Locate every uninfected red blood cell.
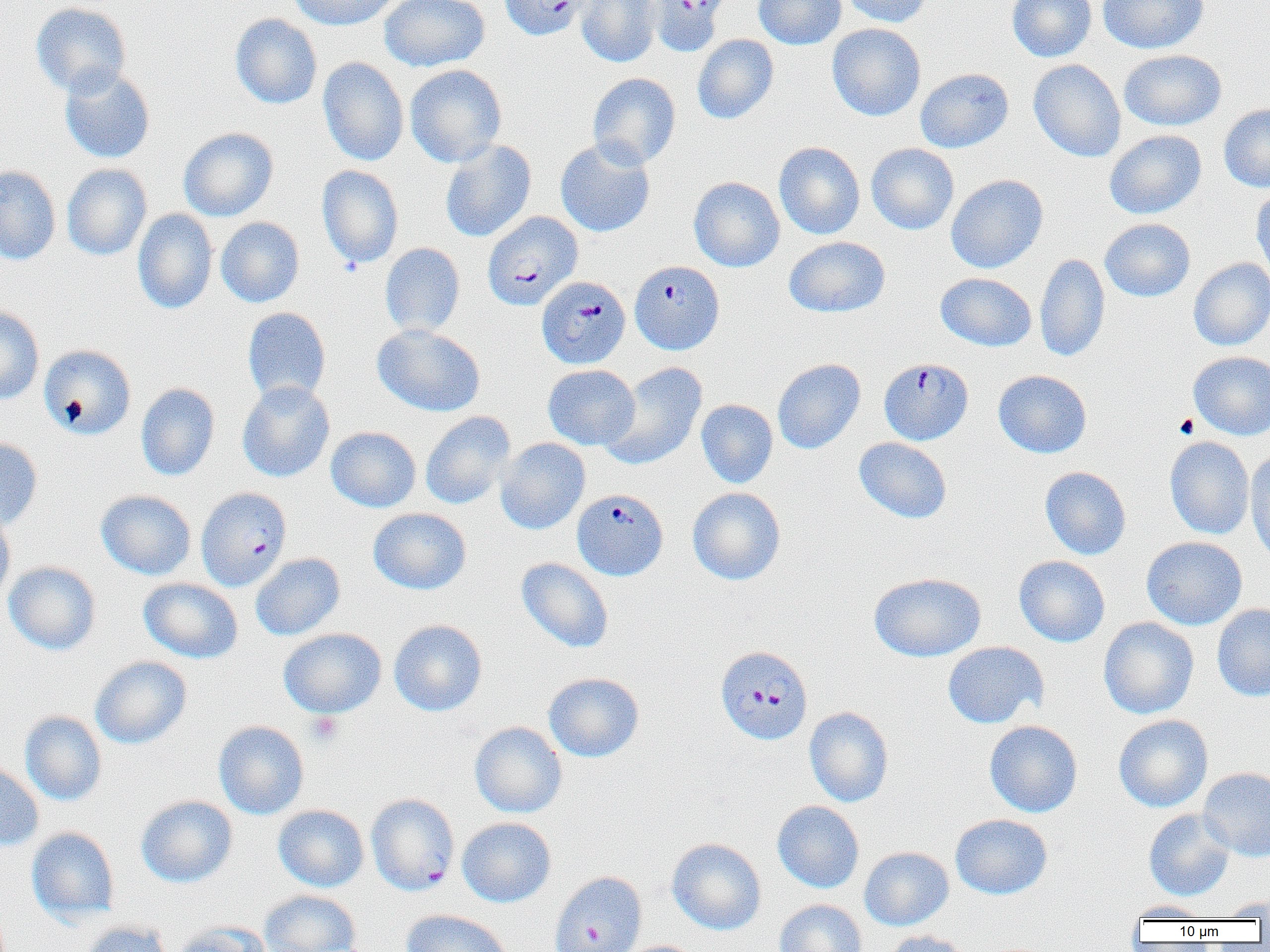
Approximate bounding boxes as (x1,y1)-(x2,y2) corner pairs in pixels.
Uninfected red blood cells: (288,0)-(402,30), (379,0)-(490,72), (577,0)-(661,68), (753,0)-(846,49), (840,0)-(931,27), (1007,0)-(1097,62), (1098,0)-(1209,54), (30,2)-(131,97), (230,14)-(322,109), (827,23)-(926,121), (692,34)-(779,124), (1119,49)-(1226,131), (318,57)-(409,167), (1028,59)-(1126,162), (405,64)-(507,167), (59,66)-(156,163), (915,68)-(1014,153), (587,73)-(681,169), (1218,104)-(1270,192), (179,127)-(278,221), (1104,129)-(1207,219), (555,138)-(655,237), (440,139)-(536,242), (774,142)-(865,239), (866,143)-(959,234), (62,163)-(151,260), (0,165)-(61,265), (317,165)-(404,268), (946,174)-(1048,273), (688,177)-(785,272), (1250,185)-(1270,279), (133,209)-(218,313), (215,217)-(304,307), (1099,218)-(1196,302), (784,237)-(890,317), (380,243)-(465,337), (1035,253)-(1110,362), (1188,257)-(1270,351), (935,272)-(1036,351), (0,306)-(44,404), (242,307)-(331,403), (372,324)-(485,417), (39,344)-(136,440), (1188,351)-(1270,440), (772,358)-(866,454), (601,361)-(708,470), (543,364)-(640,450), (993,370)-(1092,458), (237,381)-(335,483), (136,382)-(220,481), (696,399)-(778,488), (420,411)-(515,509), (326,427)-(421,512), (0,436)-(42,530), (1165,436)-(1255,539), (495,437)-(590,535), (854,437)-(952,523), (1245,449)-(1270,566), (1040,466)-(1131,560), (687,487)-(786,585), (96,490)-(196,580), (368,508)-(471,594), (0,509)-(15,607), (1141,536)-(1248,630), (250,553)-(345,640), (1014,555)-(1110,646), (516,557)-(614,653), (3,561)-(101,655), (869,572)-(986,662), (139,578)-(243,663), (1212,603)-(1270,702), (1098,616)-(1199,719), (388,619)-(487,716), (278,628)-(386,718), (942,641)-(1048,728), (90,656)-(192,749), (543,672)-(644,762), (804,706)-(894,807), (20,711)-(107,805), (1114,714)-(1213,812), (984,720)-(1083,817), (213,721)-(309,819), (469,721)-(567,818), (0,762)-(44,851), (1198,767)-(1270,862), (136,795)-(238,887), (772,801)-(865,893), (273,804)-(369,892), (1144,809)-(1235,901), (949,813)-(1052,900), (457,817)-(556,907), (26,827)-(120,924), (667,838)-(766,935), (859,847)-(954,931), (259,889)-(361,952), (1216,895)-(1270,919), (774,899)-(867,952), (1126,901)-(1215,921), (400,909)-(513,952), (80,920)-(173,952), (170,922)-(271,952), (883,930)-(978,952), (616,940)-(707,952).

slide-level diagnosis = Plasmodium falciparum
modality = light microscopy
field of view = single
magnification = 1000x
platelet locations = approximate bounding boxes as (x1,y1)-(x2,y2) corner pairs in pixels: (1173,413)-(1199,438), (306,712)-(342,746)
Plasmodium falciparum-infected red blood cell locations = approximate bounding boxes as (x1,y1)-(x2,y2) corner pairs in pixels: (500,0)-(594,41), (644,0)-(729,57), (482,211)-(583,310), (630,260)-(724,354), (537,276)-(630,369), (879,357)-(973,445), (196,487)-(292,591), (572,488)-(668,580), (715,645)-(813,745), (366,793)-(459,895), (549,871)-(647,952)
image size = 1270×952 pixels
preparation = thin blood film